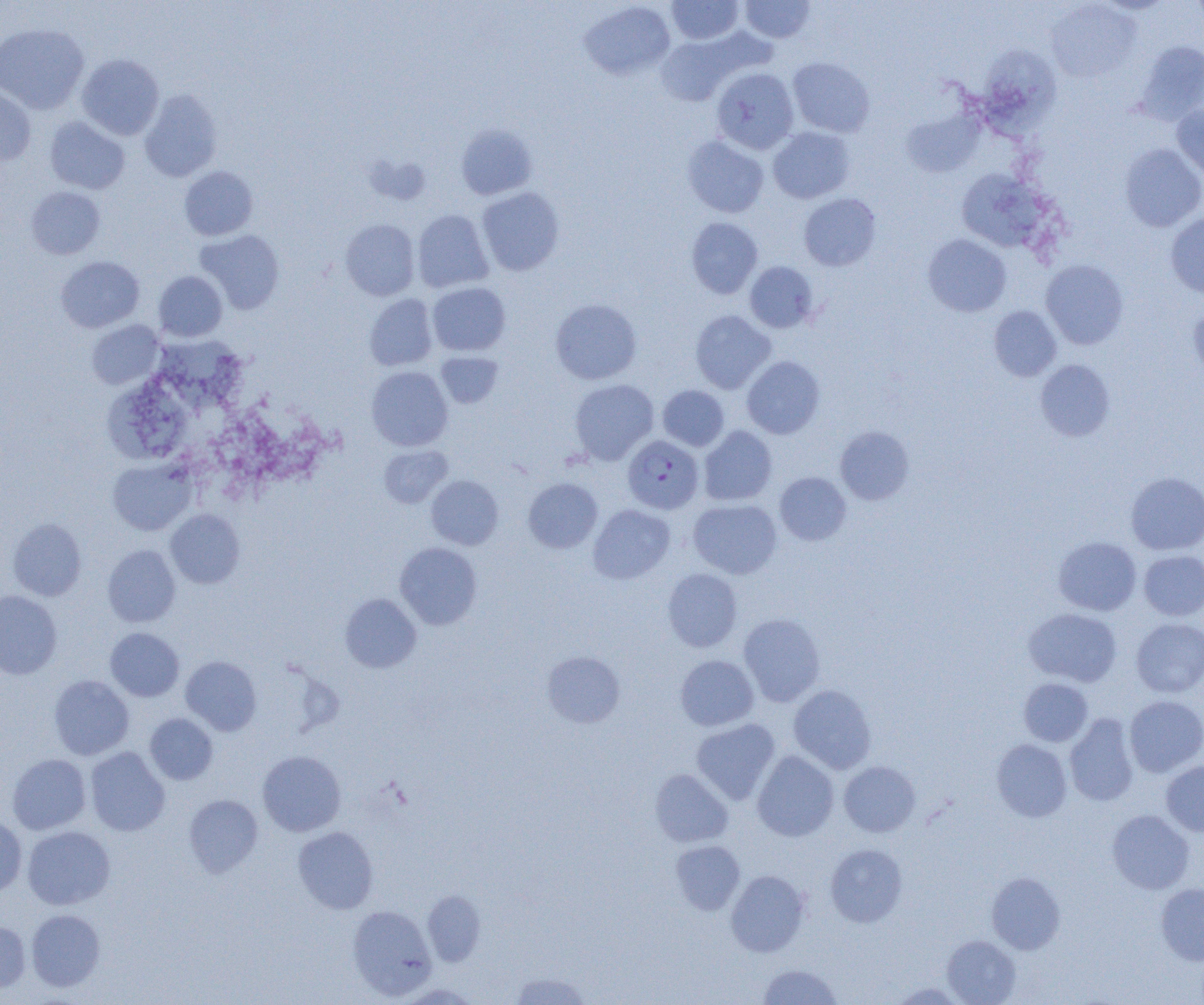

Approximate bounding boxes as (x1,y1)-(x2,y2) corner pairs in pixels. Uninfected red blood cell locations: (666,0)-(743,45), (739,0)-(815,43), (1045,1)-(1142,83), (579,2)-(676,80), (0,23)-(89,114), (656,35)-(738,106), (1135,40)-(1204,124), (979,45)-(1060,131), (77,54)-(164,140), (787,57)-(875,137), (711,67)-(799,154), (0,87)-(36,165), (139,89)-(222,182), (1172,104)-(1204,181), (899,107)-(985,177), (45,117)-(129,194), (455,124)-(537,200), (768,127)-(854,203), (682,135)-(769,218), (1120,143)-(1204,232), (363,153)-(431,206), (179,166)-(258,240), (955,168)-(1049,253), (26,186)-(105,259), (477,187)-(564,276), (799,193)-(881,271), (412,210)-(493,293), (1165,213)-(1204,298), (686,217)-(762,299), (340,219)-(420,301), (195,229)-(285,315), (922,234)-(1011,317), (56,256)-(144,333), (1040,259)-(1129,350), (745,261)-(818,333), (153,271)-(227,341), (427,283)-(510,356), (364,294)-(438,371), (550,298)-(642,385), (1187,303)-(1204,382), (989,305)-(1062,381), (690,310)-(775,394), (86,320)-(164,389), (156,335)-(244,412), (436,352)-(503,408), (742,356)-(825,439), (1035,359)-(1115,441), (366,366)-(453,451), (569,379)-(658,465), (657,385)-(729,451), (102,390)-(189,460), (699,426)-(777,506), (835,426)-(914,505), (379,445)-(453,507), (107,458)-(196,535), (1125,471)-(1204,555), (774,472)-(851,546), (426,475)-(503,549), (523,478)-(603,553), (688,499)-(781,578), (588,504)-(675,584), (165,509)-(245,588), (7,518)-(86,601), (1053,536)-(1141,615), (394,542)-(482,629), (102,544)-(180,627), (1139,550)-(1204,620), (662,568)-(742,652), (0,590)-(62,679), (340,593)-(422,673), (1024,607)-(1121,687), (738,613)-(826,706), (1131,618)-(1204,697), (105,628)-(184,701), (541,650)-(625,728), (675,655)-(759,730), (181,656)-(261,735), (49,675)-(134,759), (1019,678)-(1093,746), (788,684)-(876,774), (1124,695)-(1204,776), (145,713)-(218,784), (1065,714)-(1139,807), (691,718)-(780,805), (991,739)-(1072,822), (85,747)-(170,836), (258,750)-(346,836), (752,750)-(839,841), (7,753)-(91,834), (839,761)-(921,837), (1161,761)-(1204,836), (650,769)-(733,847), (183,794)-(263,878), (1107,809)-(1195,894), (0,814)-(27,896), (22,826)-(115,910), (293,826)-(379,914), (671,840)-(745,915), (825,843)-(907,927), (726,870)-(810,956), (986,872)-(1065,954), (1156,882)-(1204,965), (422,890)-(486,966), (347,904)-(437,1000), (25,909)-(105,991), (0,920)-(31,994), (941,935)-(1021,1005), (758,964)-(842,1005), (509,972)-(592,1005), (890,981)-(967,1005), (397,983)-(481,1004). Plasmodium falciparum-infected red blood cell locations: (623,435)-(704,513). Slide-level diagnosis: Plasmodium falciparum. Optical microscopy. One field of a larger specimen. Thin blood smear. 1000x magnification. Image is 1204×1005 pixels.